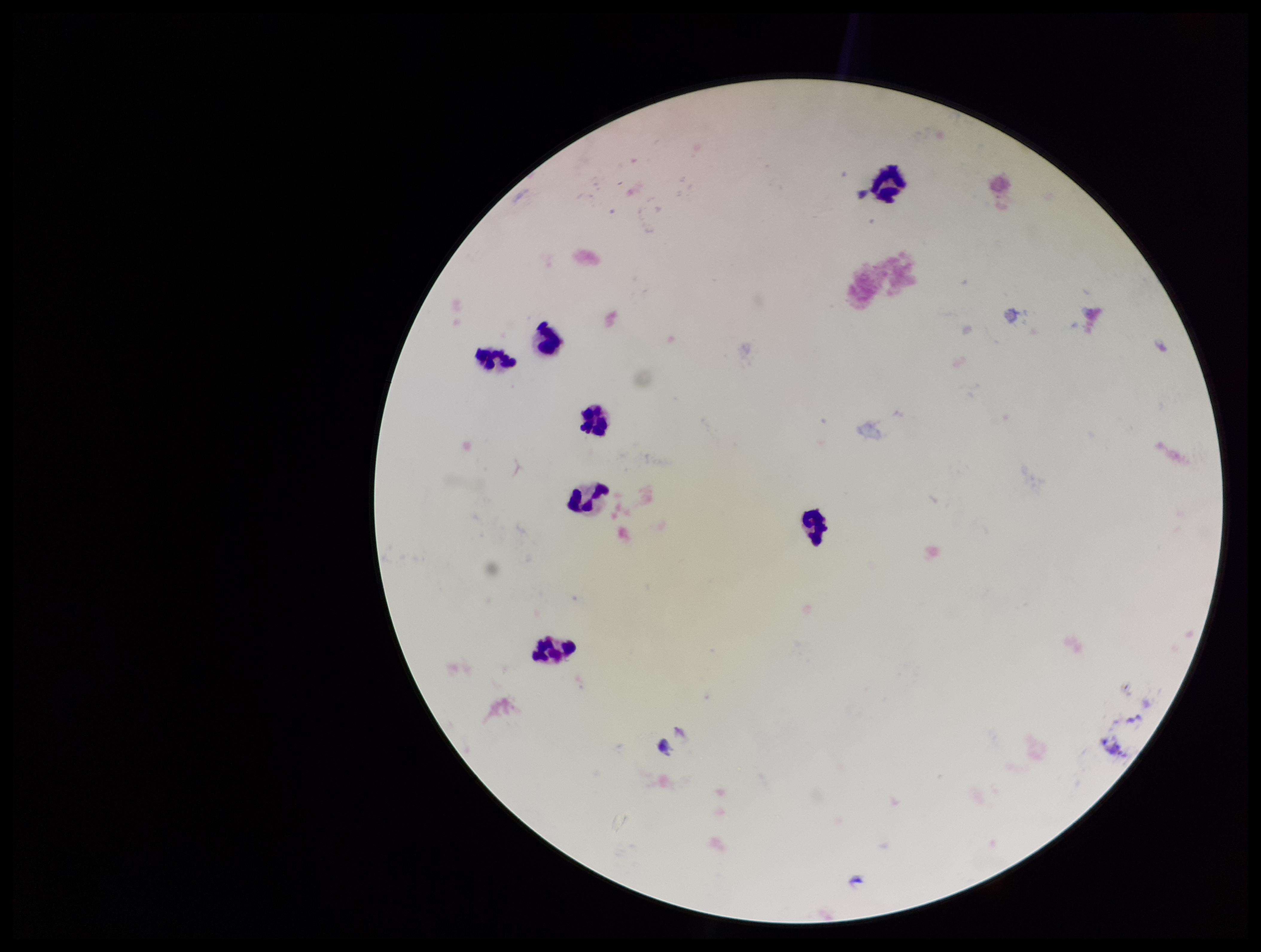
Parasite count: 0. Preparation: thick blood smear. Patient malaria status: negative. Leukocyte count: 7. Plasmodium parasites: none detected. Giemsa stain. Image is 1261×952 pixels. One field from this slide. Photographed through the microscope eyepiece with a smartphone camera.